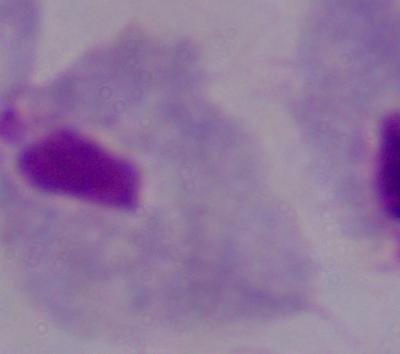
magnification = 1000x
modality = photomicrograph
identification = trichomonad